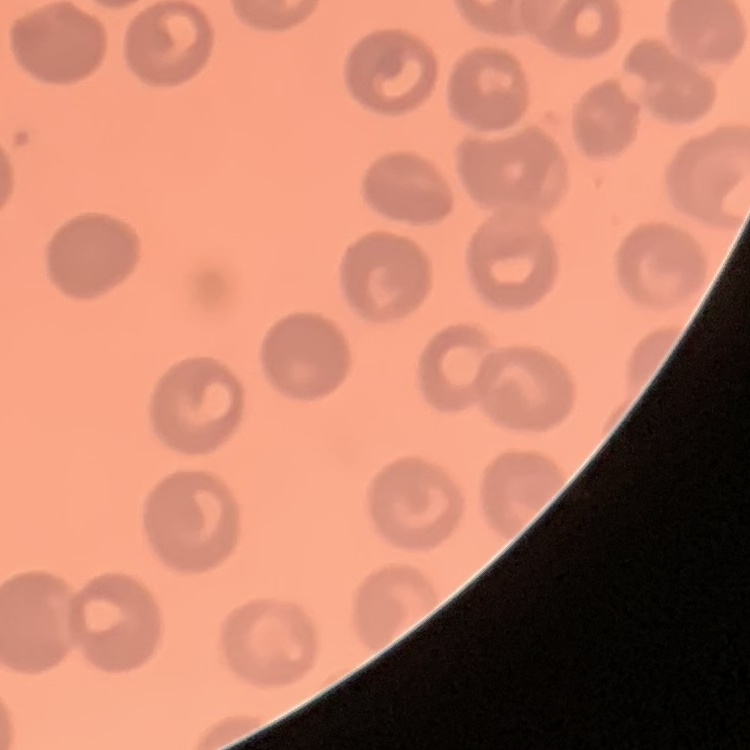

The red blood cells show no rouleaux formation. Square crop of a larger photomicrograph. Thin blood film. Field's or Giemsa stain.